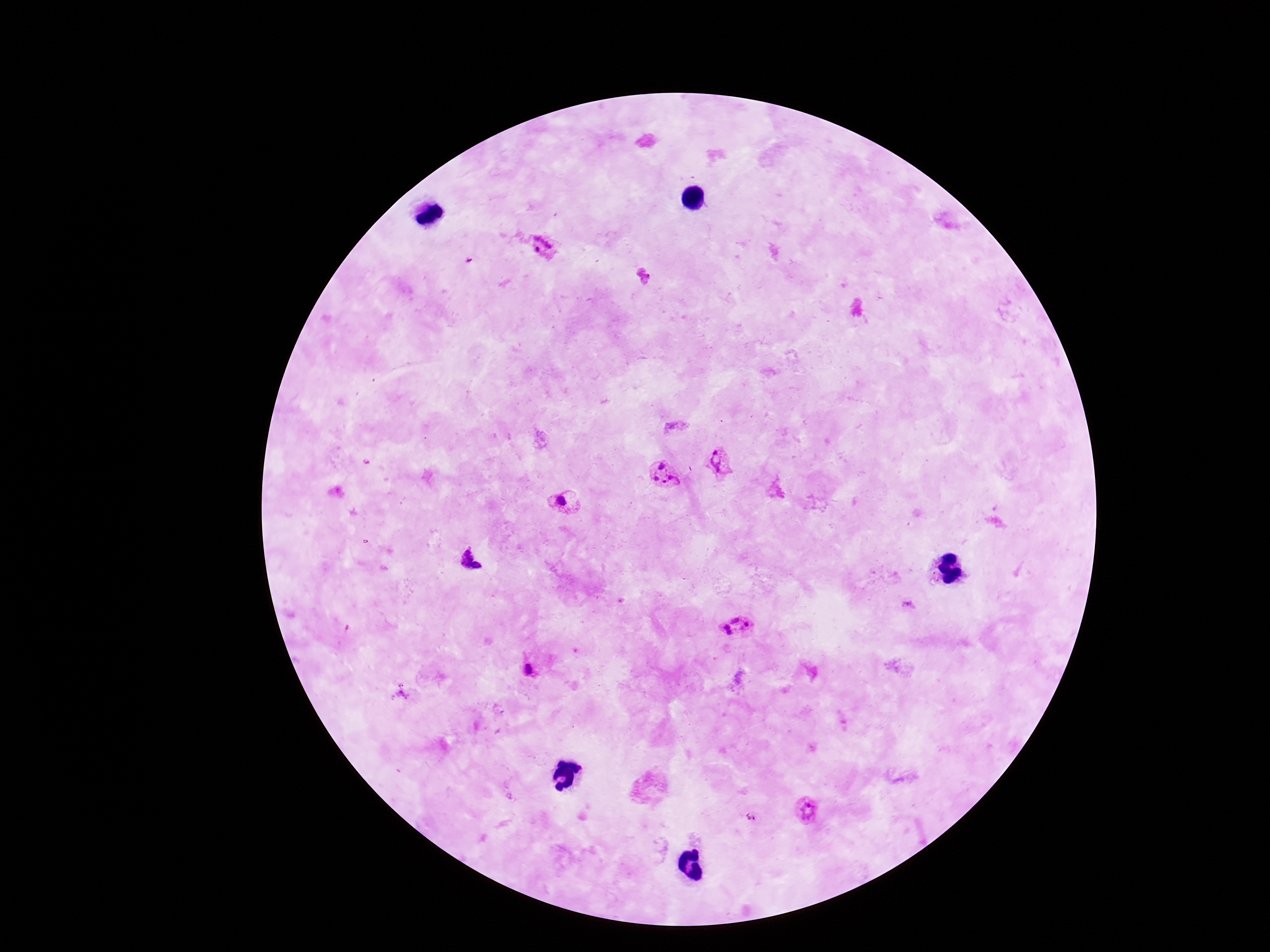
magnification = 100x
Plasmodium parasite locations = approximate object centers, in pixels from the top-left corner: (x=545, y=246), (x=718, y=465), (x=665, y=479), (x=562, y=503), (x=471, y=559), (x=907, y=606), (x=737, y=626), (x=528, y=670), (x=808, y=810), (x=752, y=818)
stain = Giemsa
image size = 1270×952 pixels
field of view = single
patient malaria status = positive
preparation = thick blood smear
capture = smartphone camera through the microscope eyepiece